Evaluate for malaria.
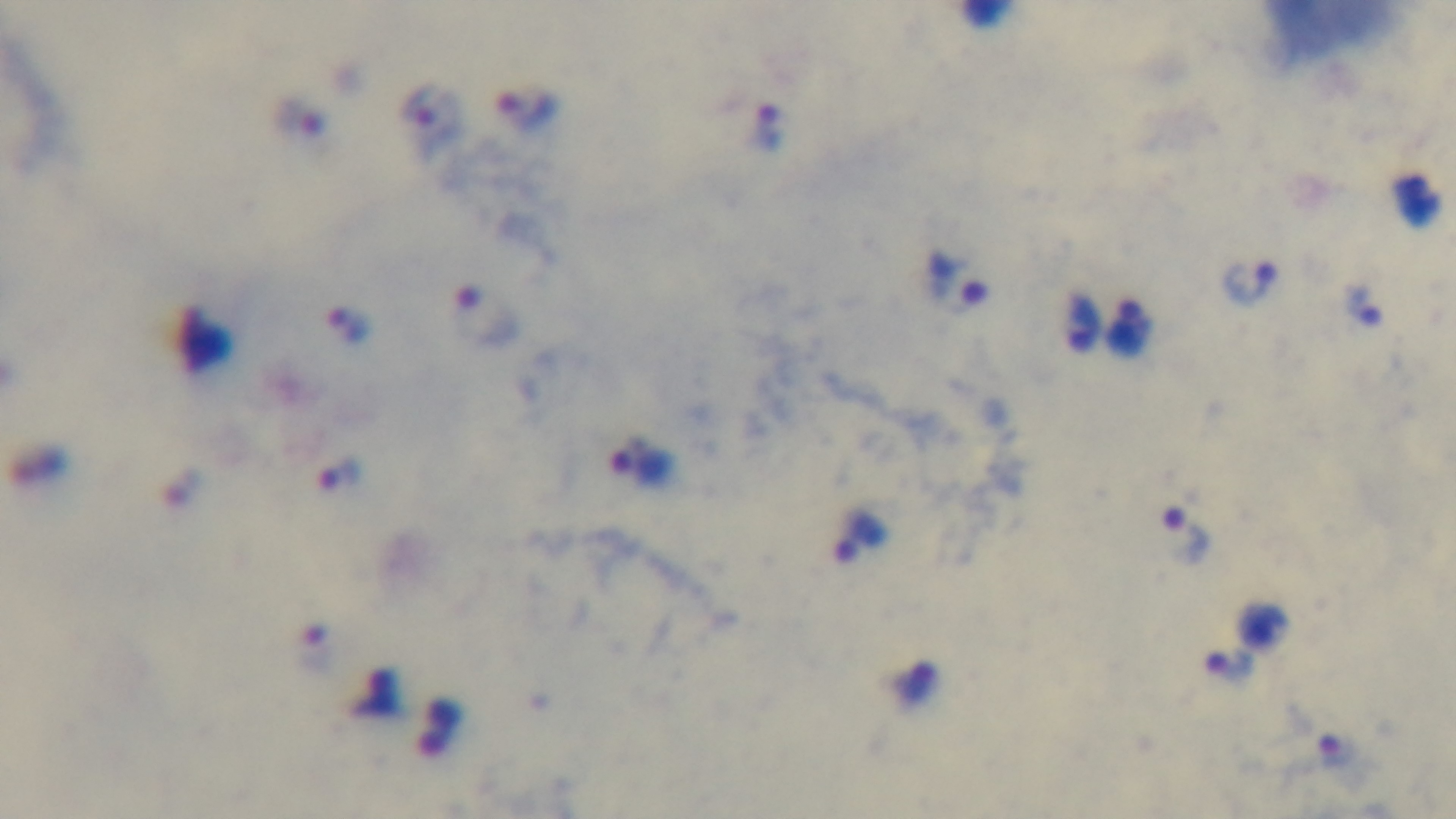
Positive.

Light microscopy. Giemsa stain. Single field of view. Captured with a mounted 4K digital camera. Preparation: thick blood film. 100x oil-immersion objective.